Give the position of every Plasmodium parasite visible.
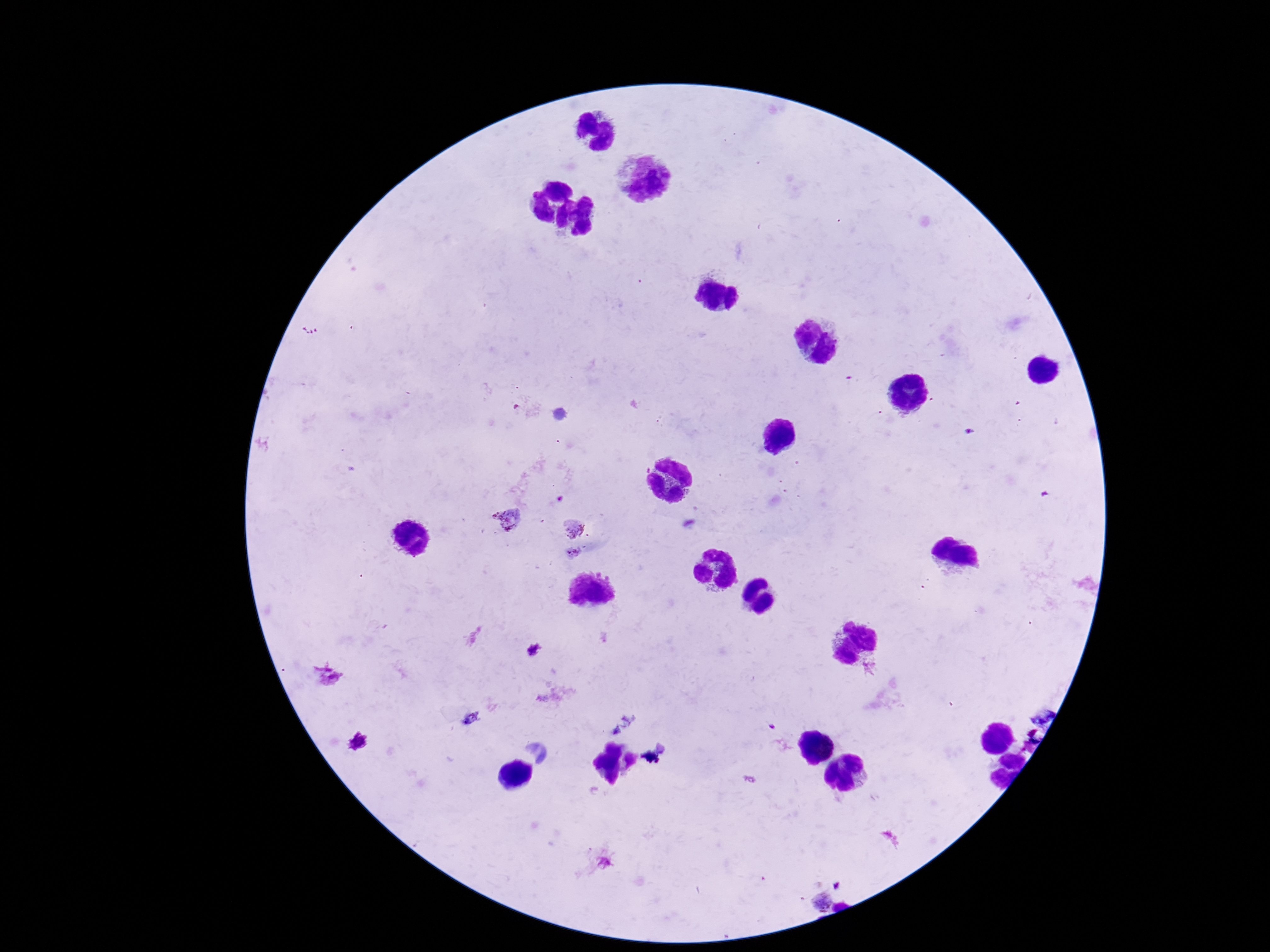

Approximate object centers, in pixels from the top-left corner.
Plasmodium parasites: (x=505, y=519), (x=575, y=529).

stain = Giemsa
patient malaria status = positive
magnification = 100x
image size = 1270×952 pixels
capture = smartphone camera through the microscope eyepiece
preparation = thick peripheral-blood smear
field of view = single